Report the malaria status of this cell.
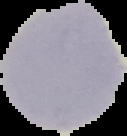
Uninfected.

Image is 127×136 pixels. From a thin blood smear. Cell region segmented out of the field of view; the surrounding area is masked to black.